Outline each Plasmodium vivax-infected red blood cell.
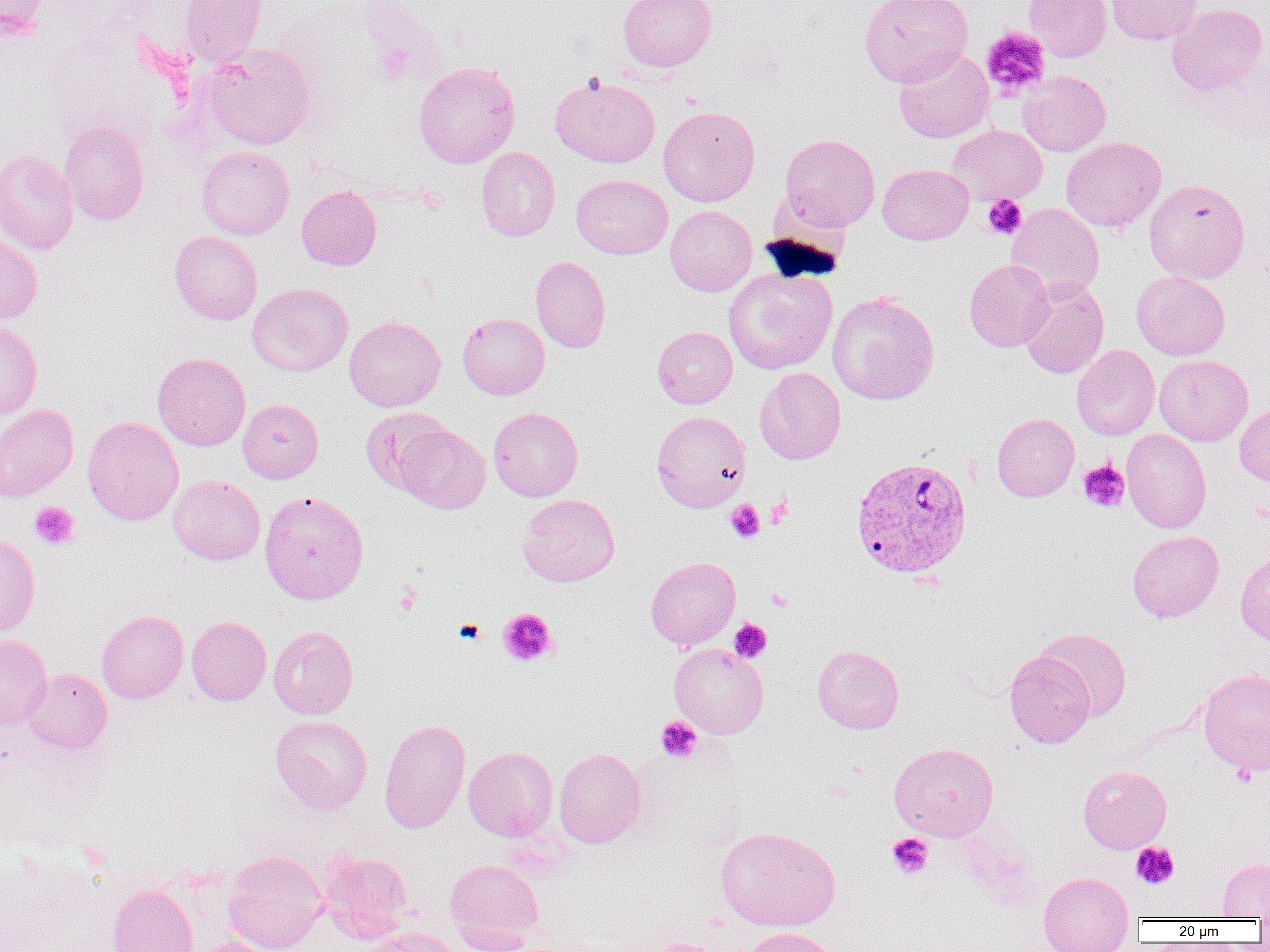
Approximate bounding boxes as [x1, y1, x2, y2] in pixels.
Plasmodium vivax-infected red blood cells: [850, 455, 973, 579].

Platelet locations: [980, 27, 1051, 98], [981, 194, 1027, 239], [1078, 460, 1130, 513], [766, 496, 792, 528], [725, 499, 765, 543], [29, 501, 80, 551], [393, 582, 423, 615], [767, 587, 793, 611], [498, 607, 558, 667], [729, 618, 772, 662], [453, 619, 486, 645], [656, 716, 702, 763], [1231, 763, 1257, 787], [887, 833, 933, 879], [1131, 842, 1179, 890]. Uninfected red blood cell locations: [0, 0, 49, 41], [180, 0, 267, 67], [618, 0, 716, 73], [860, 0, 973, 87], [1024, 0, 1111, 62], [1106, 0, 1203, 45], [1167, 3, 1268, 95], [202, 43, 316, 150], [894, 48, 994, 143], [414, 61, 520, 169], [1018, 71, 1110, 156], [550, 75, 660, 168], [659, 106, 760, 206], [58, 120, 149, 225], [946, 125, 1047, 205], [780, 134, 880, 230], [1060, 136, 1166, 232], [197, 146, 295, 240], [476, 146, 560, 241], [0, 149, 79, 255], [877, 164, 974, 244], [571, 174, 673, 259], [1144, 179, 1251, 284], [296, 185, 382, 269], [1006, 203, 1105, 300], [665, 205, 757, 296], [0, 230, 43, 325], [169, 231, 262, 325], [531, 256, 611, 353], [964, 259, 1054, 352], [723, 267, 837, 375], [1131, 271, 1230, 360], [1020, 278, 1109, 379], [247, 282, 353, 376], [827, 292, 939, 405], [457, 313, 549, 399], [344, 316, 445, 411], [0, 321, 43, 419], [652, 326, 738, 408], [1072, 345, 1160, 440], [152, 352, 250, 451], [1154, 354, 1253, 446], [755, 368, 846, 464], [238, 399, 324, 483], [1234, 403, 1270, 486], [0, 404, 78, 502], [488, 407, 583, 501], [360, 408, 451, 494], [651, 410, 751, 512], [992, 413, 1079, 502], [82, 416, 184, 525], [395, 424, 490, 513], [1121, 428, 1211, 533], [168, 474, 265, 565], [259, 490, 369, 604], [518, 494, 620, 587], [1127, 530, 1224, 622], [0, 533, 40, 637], [1235, 551, 1270, 647], [645, 556, 741, 650], [96, 610, 188, 704], [186, 616, 272, 706], [268, 625, 358, 719], [1035, 628, 1132, 720], [0, 634, 53, 730], [669, 644, 769, 738], [813, 645, 904, 734], [1004, 651, 1095, 748], [22, 668, 112, 754], [1198, 668, 1270, 776], [271, 715, 372, 814], [379, 718, 471, 834], [889, 742, 998, 841], [463, 746, 558, 840], [554, 748, 646, 848], [1078, 764, 1172, 854], [716, 826, 841, 932], [317, 849, 413, 942], [223, 850, 328, 952], [1218, 858, 1270, 920], [445, 859, 544, 951], [1038, 872, 1134, 950], [107, 884, 198, 952], [356, 927, 463, 952], [743, 927, 838, 952], [190, 938, 281, 952], [640, 938, 732, 952]. Slide-level diagnosis: Plasmodium vivax. One field of a larger specimen. Image is 1270×952 pixels. Captured at 1000x magnification. Optical microscopy. Thin blood film.